Identify the parasite.
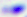
This is Toxoplasma gondii.

400x magnification. Micrograph.